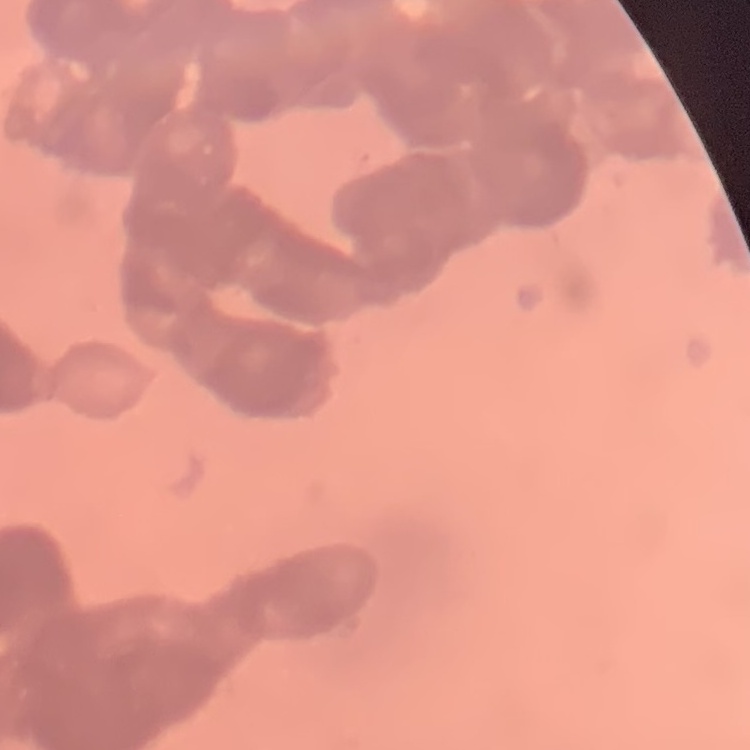 The red blood cells exhibit rouleaux formation. One tile cut from a larger photomicrograph. Thin blood film. Stained with either Field's or Giemsa.